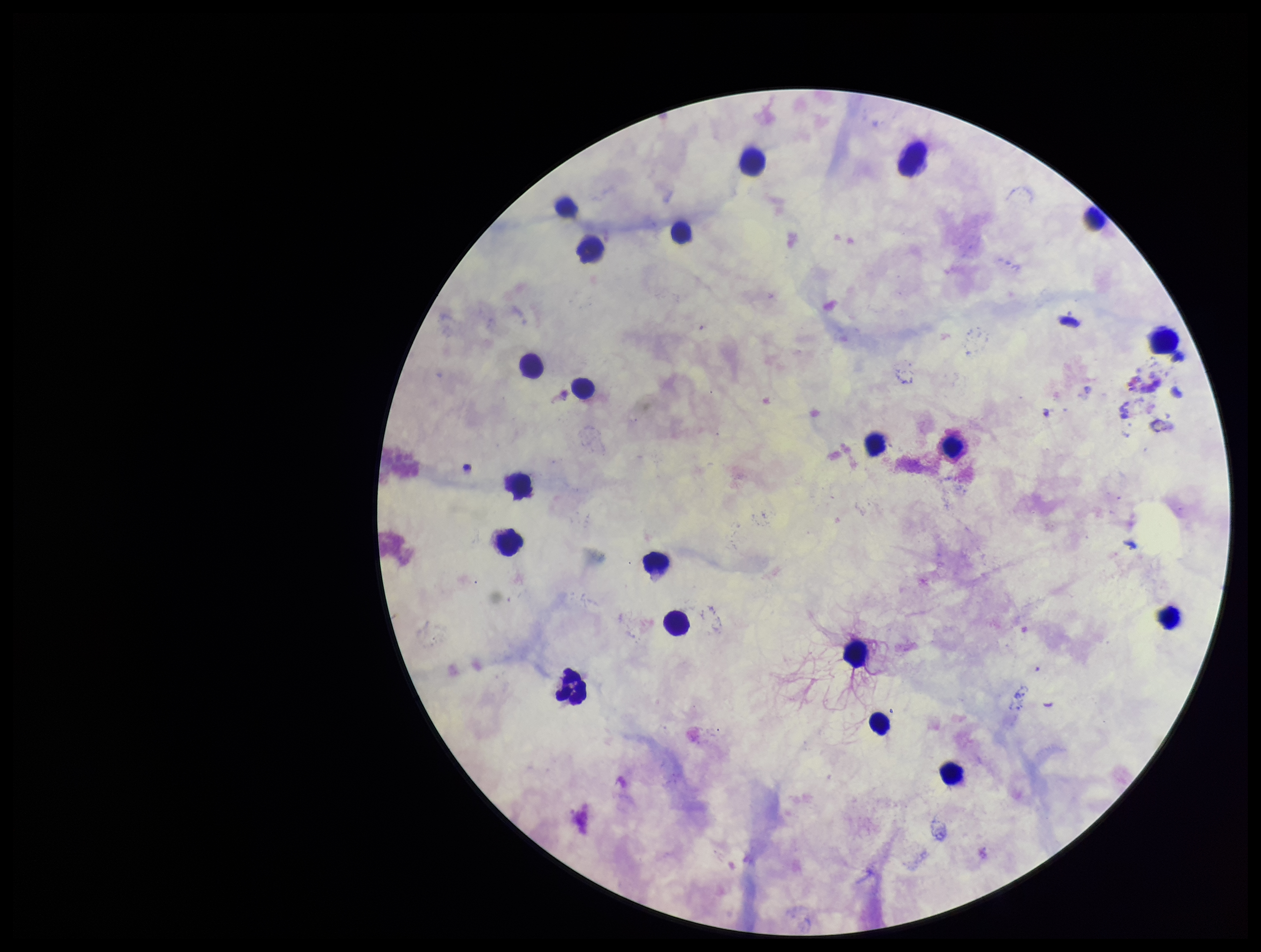

capture = smartphone photograph through the microscope eyepiece
stain = Giemsa
parasite count = 0
field of view = single
image size = 1261×952 pixels
patient malaria status = negative
leukocyte count = 23
Plasmodium parasites = none detected
preparation = thick blood smear